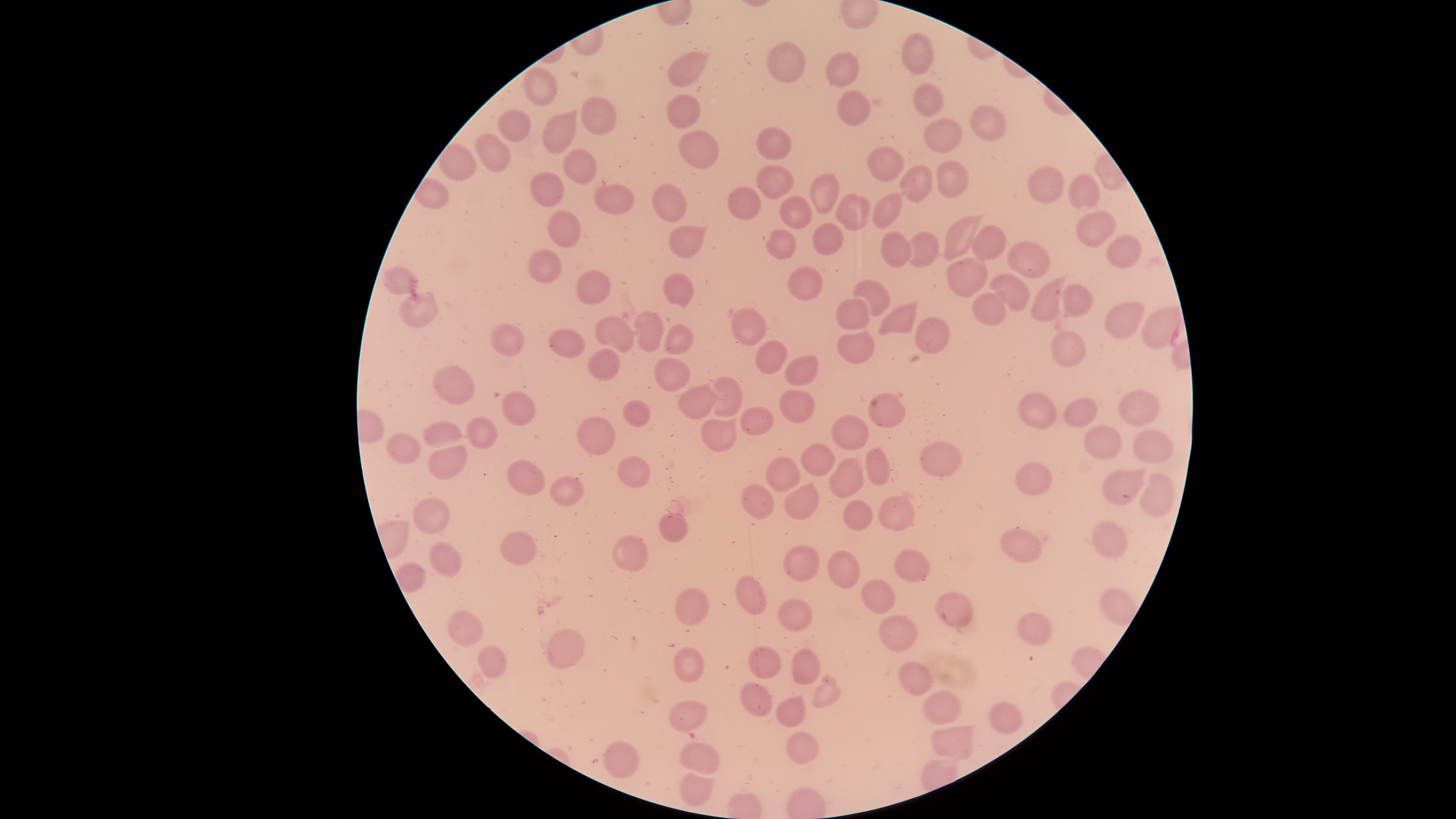

Approximate bounding boxes as [left, top, right, bottom] in pixels. Uninfected red blood cells: [903, 33, 936, 73], [767, 42, 805, 84], [667, 51, 705, 89], [825, 52, 859, 87], [525, 68, 558, 105], [912, 82, 945, 117], [837, 91, 871, 126], [667, 95, 699, 129], [581, 96, 619, 135], [969, 106, 1006, 141], [498, 112, 530, 140], [541, 113, 576, 153], [923, 118, 963, 154], [756, 128, 792, 160], [679, 130, 720, 169], [475, 134, 511, 171], [439, 143, 476, 180], [868, 147, 907, 182], [563, 149, 597, 184], [936, 160, 970, 199], [757, 164, 794, 200], [1027, 166, 1066, 203], [901, 167, 932, 202], [531, 171, 564, 207], [811, 174, 840, 214], [1070, 175, 1100, 209], [594, 182, 634, 217], [652, 184, 685, 222], [727, 187, 761, 220], [873, 193, 903, 228], [835, 194, 872, 231], [781, 197, 812, 230], [548, 211, 581, 247], [1077, 212, 1116, 246], [944, 216, 980, 261], [812, 222, 845, 257], [969, 224, 1007, 263], [670, 225, 706, 259], [765, 230, 798, 260], [906, 230, 940, 268], [880, 231, 913, 268], [1108, 236, 1142, 269], [1008, 242, 1050, 279], [528, 250, 561, 283], [947, 258, 988, 296], [787, 265, 823, 301], [384, 267, 417, 294], [576, 269, 611, 305], [661, 273, 695, 309], [989, 274, 1029, 312], [1031, 278, 1064, 322], [854, 280, 892, 317], [1062, 285, 1094, 318], [399, 293, 439, 328], [973, 293, 1006, 326], [835, 297, 870, 331], [879, 301, 917, 338], [1105, 302, 1143, 338], [1139, 306, 1179, 351], [731, 308, 766, 347], [634, 312, 664, 352], [595, 318, 635, 353], [913, 318, 951, 355], [493, 324, 525, 355], [665, 324, 693, 354], [837, 326, 875, 365], [548, 330, 586, 358], [1053, 331, 1086, 366], [755, 340, 787, 374], [588, 348, 621, 381], [787, 356, 818, 386], [655, 358, 690, 392], [433, 367, 475, 405], [711, 376, 744, 418], [678, 384, 720, 421], [780, 390, 813, 422], [503, 392, 536, 425], [1019, 392, 1056, 429], [1120, 392, 1160, 425], [869, 393, 906, 428], [1065, 398, 1098, 426], [623, 400, 651, 427], [739, 406, 774, 436], [702, 415, 738, 452], [831, 416, 869, 450], [577, 417, 617, 456], [468, 418, 497, 449], [423, 420, 462, 448], [1083, 425, 1122, 460], [1135, 430, 1174, 463], [386, 434, 420, 463], [802, 443, 835, 477], [921, 443, 963, 478], [428, 444, 466, 479], [866, 449, 892, 486], [619, 456, 651, 487], [767, 457, 800, 492], [508, 459, 545, 495], [829, 461, 865, 498], [1014, 462, 1053, 495], [1103, 469, 1145, 504], [1141, 472, 1175, 517], [550, 474, 584, 507], [783, 483, 820, 519], [741, 485, 776, 521], [878, 497, 913, 530], [411, 498, 450, 535], [843, 500, 872, 531], [660, 514, 688, 542], [1094, 521, 1129, 558], [1001, 530, 1042, 561], [501, 532, 537, 565], [613, 535, 649, 571], [428, 543, 461, 576], [784, 545, 819, 581], [895, 550, 930, 582], [828, 551, 860, 589], [735, 576, 767, 614], [860, 580, 896, 615], [676, 587, 711, 626], [937, 593, 973, 628], [777, 598, 814, 631], [448, 611, 484, 646], [1018, 614, 1052, 644], [878, 615, 916, 652], [547, 629, 585, 669], [479, 646, 506, 678], [750, 646, 782, 679], [673, 647, 704, 683], [792, 651, 821, 684], [899, 662, 931, 696], [740, 682, 772, 716], [925, 691, 961, 724], [773, 697, 805, 729], [669, 700, 706, 731], [990, 702, 1023, 734], [932, 729, 973, 758], [786, 732, 818, 765], [604, 741, 640, 778], [677, 742, 720, 774], [680, 768, 713, 805]. Thin blood film. Giemsa-stained preparation. Photographed with a smartphone camera through the microscope eyepiece. Image is 1456×819 pixels. One field of view of the specimen. Presence: no malaria parasites detected. Circular visible region.